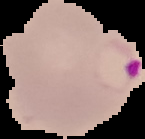 Segmented cell region on a black background. Image is 145×139 pixels. Malaria status: parasitized. From a thin blood smear.